Classify this cell by malaria status.
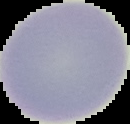
It is uninfected.

{
  "preparation": "thin blood smear",
  "image_size": "130×124 pixels",
  "image_type": "segmented cell region with the area outside set to black"
}